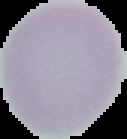

Segmented cell region on a black background. Result: no malaria parasites detected. Image is 127×139 pixels. From a thin blood film.